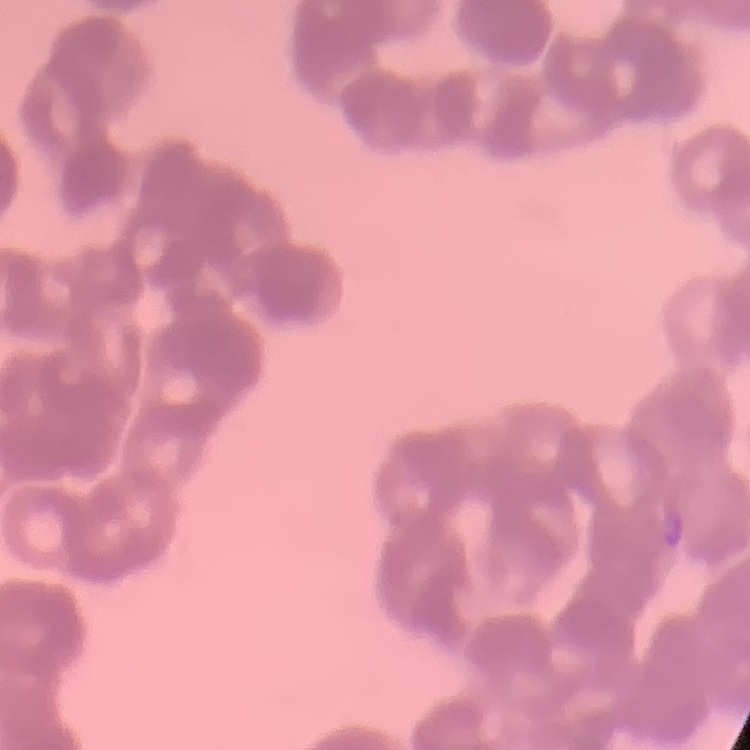
erythrocyte_morphology: rouleaux formation
preparation: thin peripheral smear
image_type: square crop of a larger photomicrograph
stain: Field's or Giemsa